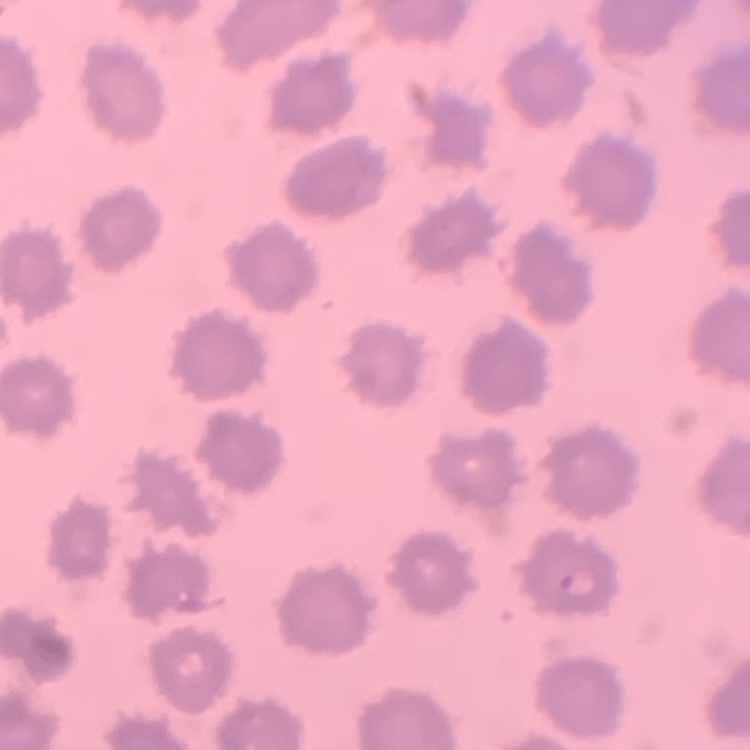

The erythrocytes show no rouleaux formation. Thin blood film. Field's or Giemsa stain. Square crop of a larger photomicrograph.